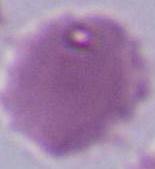
Summary:
  - Identification: red blood cell
  - Magnification: 1000x
  - Modality: photomicrograph